Locate every malaria parasite and every leukocyte.
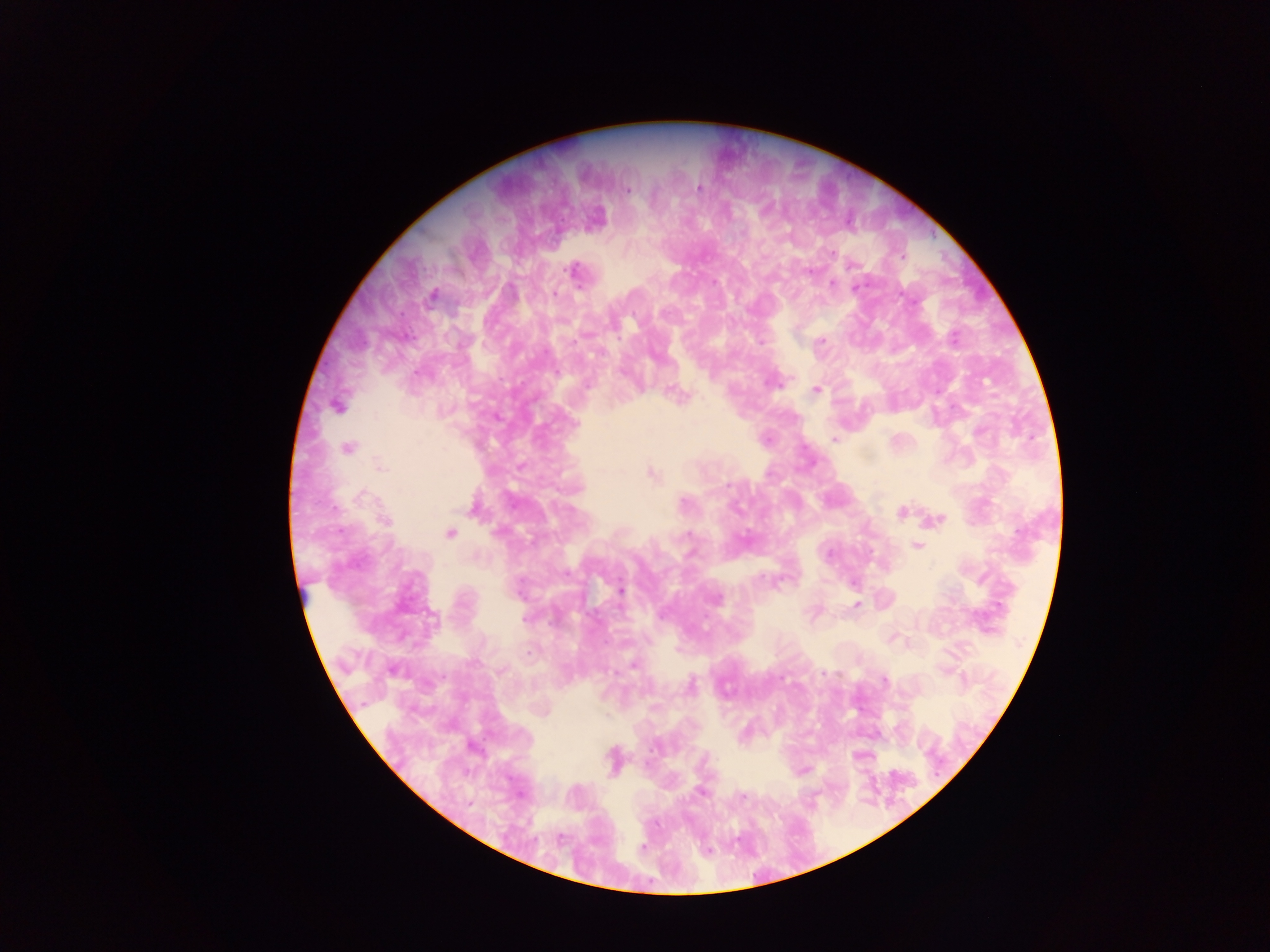
Approximate centers as (x, y) in pixels.
Malaria parasites: (698, 188), (627, 190), (832, 253), (852, 264), (574, 271), (809, 271), (832, 284), (856, 287), (554, 294), (433, 296), (954, 338), (761, 342), (821, 342), (416, 373), (774, 384), (815, 390), (675, 394), (337, 406), (834, 440), (347, 447), (380, 467), (652, 475), (729, 485), (362, 496), (684, 503), (902, 512), (940, 519), (386, 521), (450, 533), (689, 535), (917, 546), (829, 554), (621, 590), (716, 599), (857, 605), (524, 619), (633, 666), (393, 670), (824, 674), (883, 680), (691, 685), (701, 793), (742, 795), (469, 802), (560, 839), (643, 847).
No leukocytes observed.

capture: mobile-phone photograph through a microscope
field_of_view: single
image_size: 1270×952 pixels
country: Ghana
preparation: thick blood smear